Point out leukocytes.
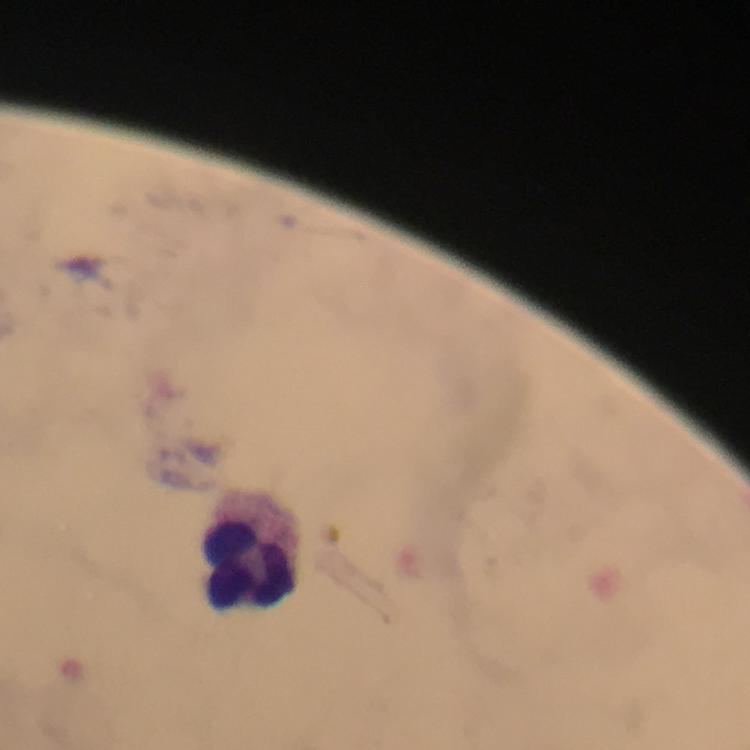
Approximate object centers, in pixels from the top-left corner.
Leukocytes: (x=251, y=563).

malaria parasites = none detected
magnification = 100x
context = from a malaria diagnostic workup
stain = Giemsa
image size = 750×750 pixels
capture = smartphone photograph through a microscope
immersion oil = applied
preparation = thick blood film
cropped from = one field of view